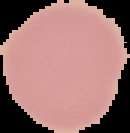

{
  "preparation": "thin blood film",
  "result": "no Plasmodium parasites seen",
  "image_type": "segmented cell region with the area outside set to black",
  "image_size": "130×133 pixels"
}